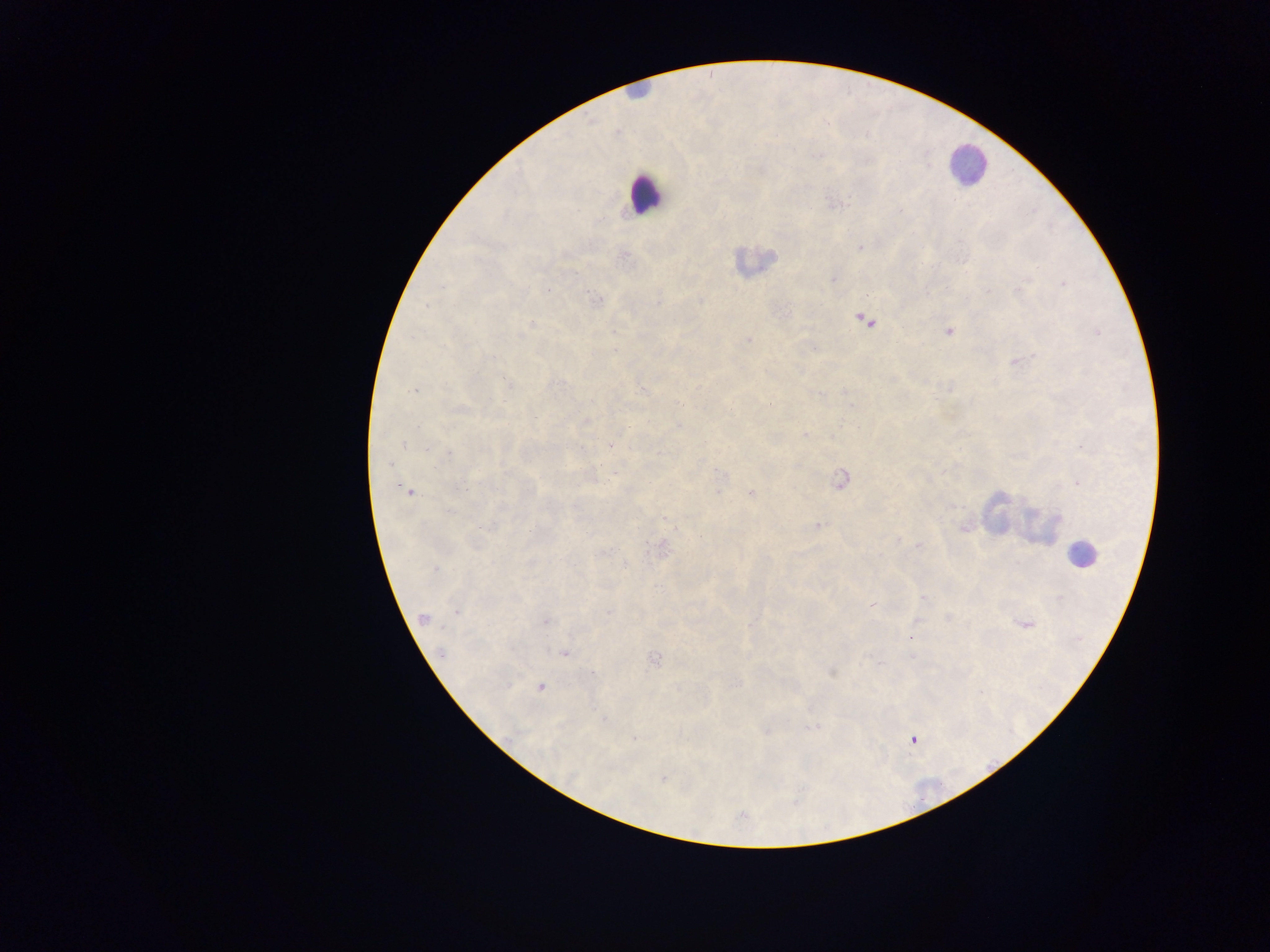 Approximate centers as x y in pixels. Leukocyte locations: 638 89; 967 163; 644 193; 754 261; 1001 514; 1029 523; 1082 554. Malaria parasite locations: 834 204; 860 248; 624 255; 1026 279; 833 280; 1063 284; 547 290; 988 291; 597 300; 700 301; 658 302; 427 306; 864 320; 532 326; 614 331; 949 332; 1098 332; 520 335; 747 340; 613 350; 491 357; 1018 362; 509 384; 643 389; 949 389; 414 390; 845 391; 848 398; 682 404; 770 404; 852 406; 461 408; 729 410; 536 417; 586 421; 678 427; 805 434; 404 444; 610 445; 428 447; 582 448; 1082 448; 448 453; 659 454; 390 465; 615 473; 719 473; 840 480; 1078 483; 399 487; 459 489; 406 491; 718 493; 751 493; 448 511; 664 519; 818 525; 493 526; 964 528; 586 533; 701 538; 899 540; 919 545; 661 549; 606 552; 879 555; 625 567; 435 569; 658 586; 923 597; 1060 597; 872 605; 457 611; 608 611; 424 618; 948 618; 546 622; 917 622; 748 624; 1025 624; 912 637; 441 652; 564 653; 654 658; 831 672; 594 674; 508 685; 540 686; 604 720; 812 728; 765 731; 634 738; 913 739; 663 779. Collected in Ghana. Photographed through a microscope with a mobile-phone camera. Single field of view. Image is 1270×952 pixels. Thick blood smear.